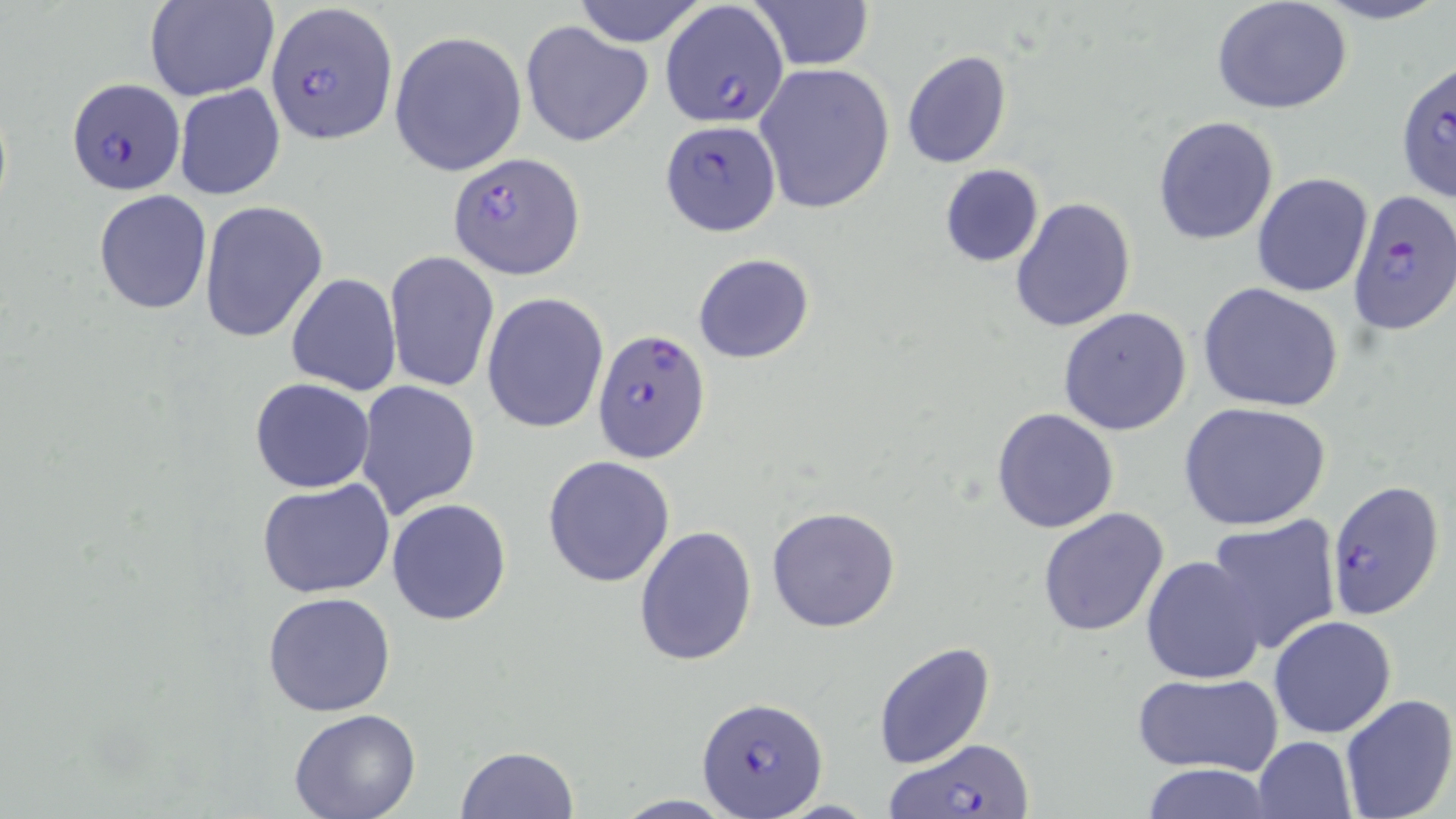

Approximate bounding boxes as (x1,y1)-(x2,y2) corner pairs in pixels. Uninfected red blood cell locations: (146,0)-(277,100), (572,0)-(709,48), (750,0)-(874,71), (1303,0)-(1452,26), (1211,1)-(1352,116), (521,21)-(653,148), (389,31)-(527,177), (902,49)-(1012,169), (754,63)-(895,214), (173,83)-(286,201), (1152,115)-(1279,247), (939,163)-(1045,267), (1251,172)-(1373,297), (93,189)-(212,315), (1010,197)-(1136,332), (198,201)-(328,343), (384,250)-(499,394), (692,253)-(814,363), (285,273)-(401,395), (1199,281)-(1346,413), (482,293)-(608,433), (1057,306)-(1191,435), (249,377)-(377,494), (355,380)-(481,518), (1178,401)-(1333,531), (991,407)-(1119,534), (543,456)-(675,588), (256,480)-(395,598), (386,497)-(512,626), (766,505)-(900,633), (1037,507)-(1169,637), (1205,517)-(1343,656), (633,525)-(758,668), (1142,555)-(1268,687), (263,591)-(398,718), (1268,615)-(1398,740), (874,642)-(996,769), (1131,671)-(1283,775), (1339,693)-(1456,819), (287,710)-(422,819), (1252,735)-(1357,819), (454,745)-(581,818), (1133,764)-(1277,819), (608,794)-(740,818). Plasmodium falciparum-infected red blood cell locations: (266,3)-(398,146), (658,3)-(789,128), (1394,59)-(1456,202), (71,76)-(192,193), (659,121)-(781,236), (448,150)-(584,279), (1347,189)-(1456,337), (593,326)-(710,463), (1327,478)-(1446,621), (697,696)-(827,818), (889,739)-(1034,818). Slide-level diagnosis: Plasmodium falciparum. May-Grünwald-Giemsa-stained preparation. Captured at 1000x magnification. Thin blood smear. Image is 1456×819 pixels. One field of a larger specimen. Optical microscopy.